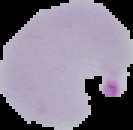

malaria status = parasitized
image size = 133×130 pixels
preparation = thin blood smear
image type = segmented cell region with the area outside set to black